Assess this cell for malaria.
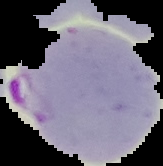

Parasitized.

Image is 163×166 pixels. From a thin blood smear. The area outside the segmented cell region is set to black.